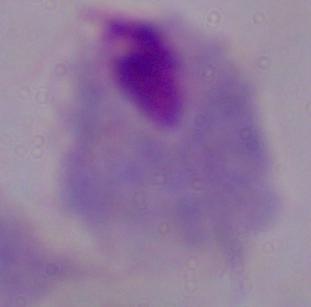
Photomicrograph. A trichomonad is shown. Captured at 1000x magnification.